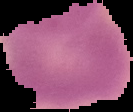
result = no Plasmodium parasites seen
preparation = thin blood smear
image size = 133×112 pixels
image type = cell region segmented out of the field of view; surrounding area masked to black